State the blood parasite species.
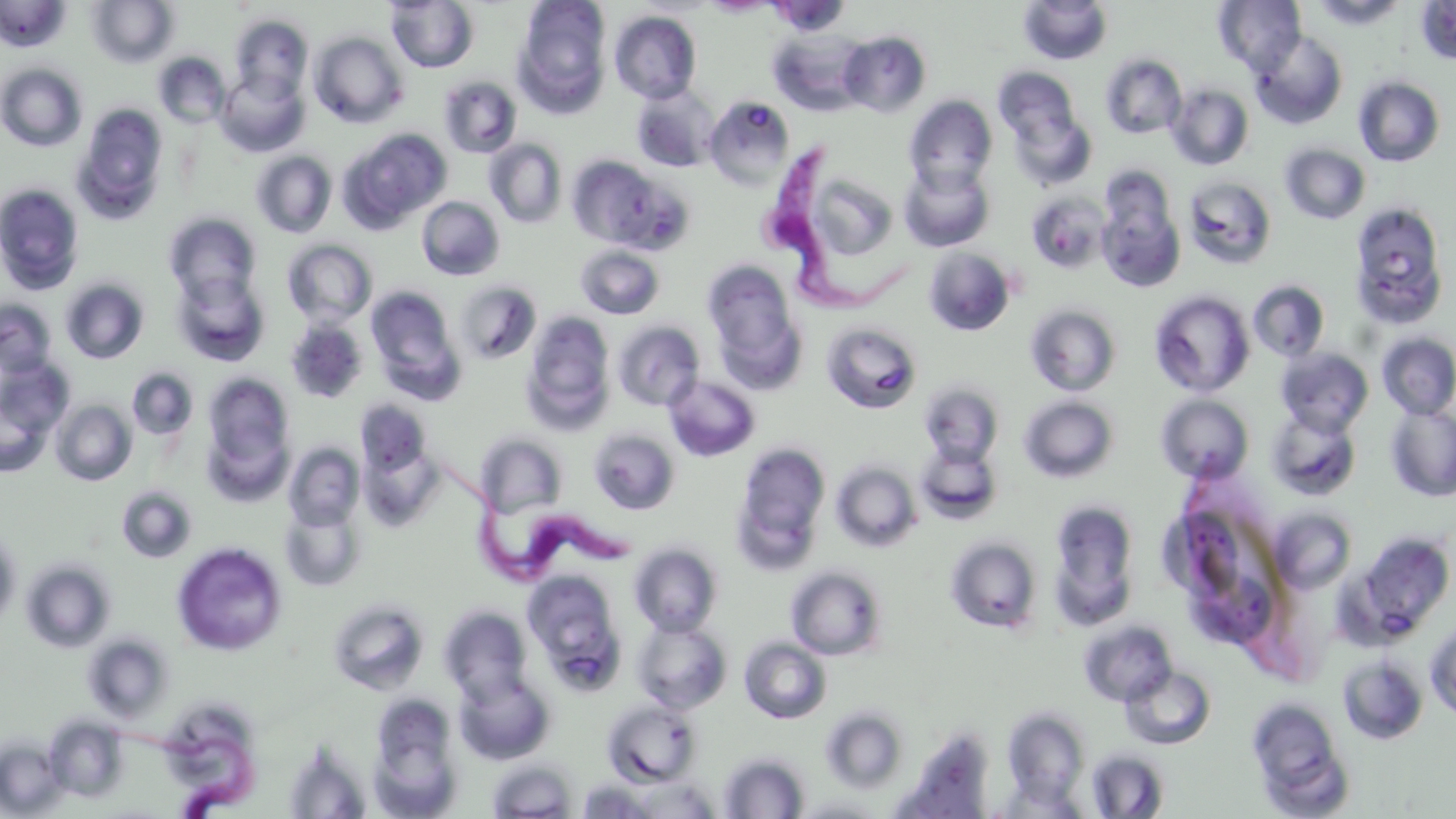

Trypanosoma brucei.

stain: May-Grünwald-Giemsa
image_size: 1456×819 pixels
trypanosoma_brucei_locations: 'approximate bounding boxes as [x1, y1, x2, y2] in pixels: [757, 144, 924, 320], [420, 432, 633, 586], [87, 722, 279, 819]'
preparation: thin blood film
field_of_view: single
modality: light microscopy
magnification: 1000x
uninfected_red_blood_cell_locations: 'approximate bounding boxes as [x1, y1, x2, y2] in pixels: [87, 0, 179, 68], [702, 0, 778, 16], [1214, 0, 1306, 75], [1309, 0, 1409, 29], [0, 1, 70, 52], [386, 1, 479, 72], [514, 1, 612, 113], [766, 1, 850, 37], [1018, 1, 1113, 65], [1414, 1, 1456, 66], [609, 11, 701, 104], [229, 15, 313, 102], [771, 30, 866, 115], [1250, 30, 1348, 130], [838, 31, 931, 117], [309, 32, 407, 128], [154, 53, 231, 128], [1100, 53, 1187, 139], [0, 63, 87, 152], [993, 67, 1081, 148], [216, 71, 309, 157], [439, 76, 522, 158], [1353, 76, 1446, 167], [1166, 83, 1254, 170], [631, 84, 720, 172], [704, 95, 796, 188], [904, 96, 997, 190], [72, 103, 169, 225], [1008, 107, 1097, 190], [343, 128, 452, 231], [484, 138, 568, 228], [1280, 143, 1371, 224], [251, 151, 337, 238], [567, 156, 669, 249], [898, 163, 994, 252], [794, 168, 901, 267], [1095, 175, 1186, 293], [1183, 175, 1278, 270], [0, 183, 85, 295], [1025, 191, 1110, 273], [417, 196, 505, 281], [1349, 202, 1451, 328], [163, 212, 261, 304], [282, 239, 378, 328], [575, 244, 665, 319], [923, 247, 1016, 336], [702, 260, 804, 379], [171, 270, 270, 366], [60, 278, 149, 364], [453, 280, 542, 365], [1248, 280, 1330, 362], [367, 286, 461, 393], [1149, 290, 1255, 398], [0, 299, 58, 380], [1025, 304, 1122, 396], [521, 312, 616, 431], [284, 319, 368, 404], [612, 321, 705, 411], [821, 321, 923, 414], [1376, 332, 1456, 419], [1276, 347, 1374, 436], [1, 360, 73, 442], [127, 368, 198, 440], [202, 372, 295, 486], [664, 375, 761, 462], [919, 381, 1004, 466], [0, 387, 54, 478], [1156, 394, 1254, 484], [1018, 396, 1119, 483], [51, 400, 136, 486], [355, 401, 432, 478], [1384, 404, 1456, 502], [1266, 409, 1361, 502], [589, 428, 680, 515], [475, 433, 568, 519], [915, 441, 1003, 525], [732, 442, 831, 568], [283, 443, 364, 530], [359, 444, 443, 531], [831, 460, 923, 553], [117, 486, 197, 563], [1048, 500, 1140, 625], [279, 501, 366, 592], [1269, 508, 1358, 594], [0, 529, 22, 629], [1351, 530, 1454, 642], [945, 535, 1043, 634], [172, 541, 288, 657], [629, 542, 723, 637], [20, 559, 116, 653], [785, 565, 888, 660], [522, 569, 626, 685], [328, 598, 430, 695], [439, 605, 533, 702], [632, 617, 732, 714], [1078, 618, 1178, 706], [1425, 620, 1456, 722], [82, 633, 175, 723], [739, 637, 833, 724], [1337, 654, 1428, 745], [1121, 665, 1216, 750], [454, 670, 556, 766], [369, 693, 460, 802], [1246, 697, 1351, 814], [602, 699, 702, 786], [154, 705, 261, 812], [820, 707, 908, 794], [1002, 708, 1091, 806], [43, 714, 131, 803], [0, 737, 68, 817], [282, 742, 372, 818], [1086, 748, 1169, 818], [717, 751, 811, 818], [487, 759, 578, 819], [630, 776, 722, 818], [576, 778, 662, 818], [789, 796, 891, 818]'